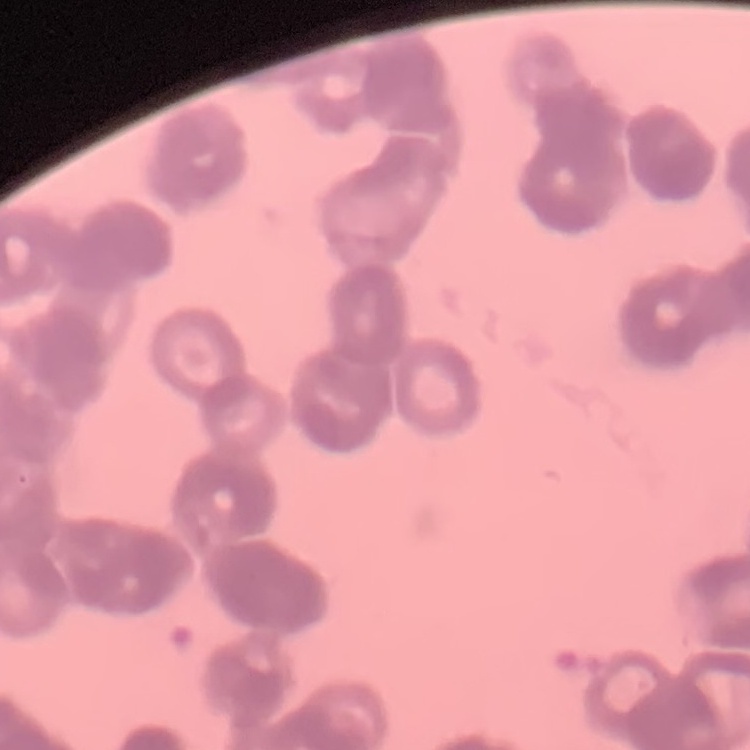 The red blood cells show rouleaux formation. Thin peripheral smear. Square crop of a larger photomicrograph. Stained with either Field's or Giemsa.